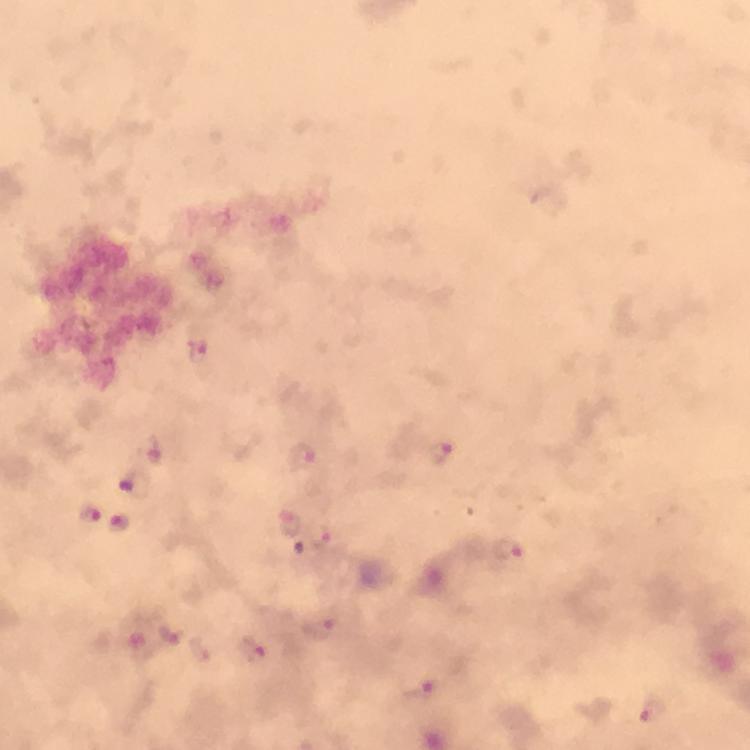

Plasmodium parasite locations = approximate centers as {x, y} in pixels: {199, 351}, {441, 452}, {300, 457}, {135, 484}, {89, 514}, {119, 522}, {290, 523}, {509, 550}, {318, 629}, {173, 632}, {252, 648}, {420, 688}, {654, 712}
context = from a diagnostic examination for malaria
image size = 750×750 pixels
preparation = thick blood smear
stain = Giemsa
magnification = 100x
capture = smartphone photograph through a microscope
immersion oil = applied
cropped from = one field of view